Assess this cell for malaria.
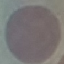

Uninfected.

image type = automatically extracted cell patch, resized to 64 × 64 pixels
stain = Giemsa
capture = smartphone through the microscope eyepiece
preparation = thin smear